Comment on the morphology of the red blood cells.
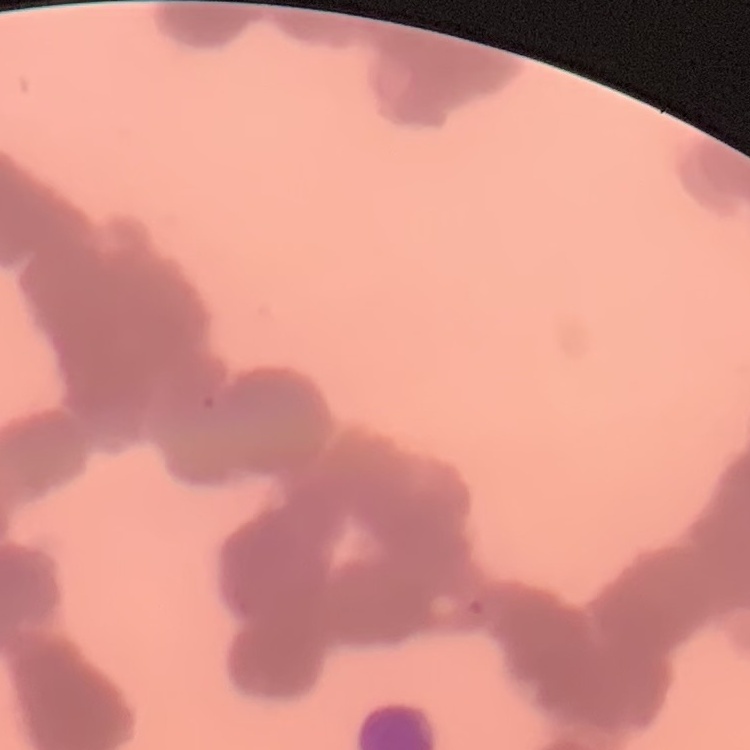

Rouleaux formation.

Stained with either Field's or Giemsa. Square crop of a larger photomicrograph. Thin blood smear.